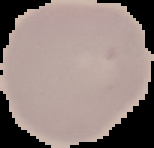
From a thin blood smear. Malaria status: uninfected. The area outside the segmented cell region is set to black. Image is 154×148 pixels.